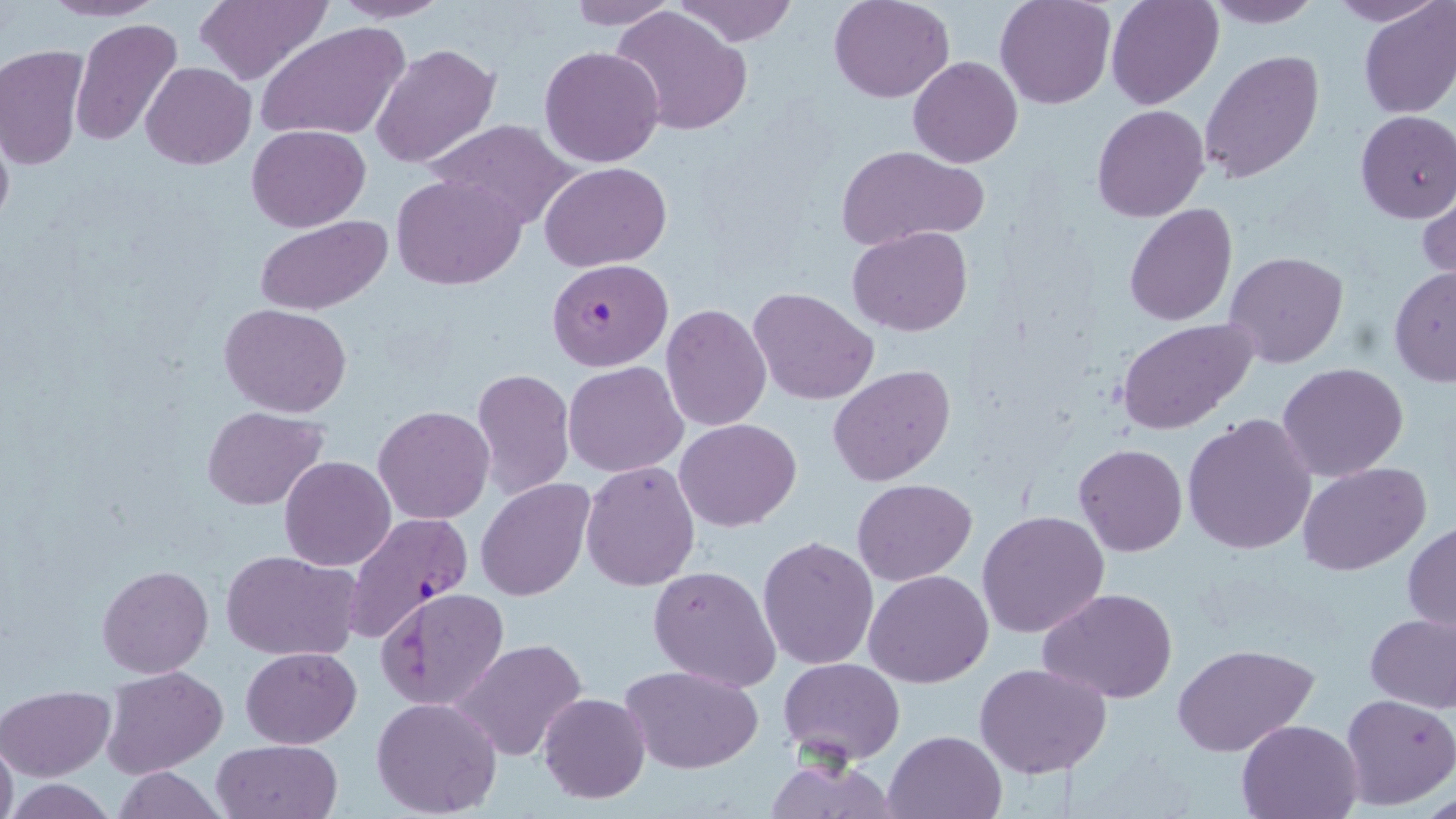 Approximate bounding boxes as [x1, y1, x2, y2] in pixels. Uninfected red blood cell locations: [38, 0, 166, 22], [193, 0, 330, 86], [328, 0, 454, 23], [674, 0, 800, 46], [830, 0, 955, 103], [995, 0, 1114, 110], [1106, 0, 1222, 110], [1203, 0, 1326, 28], [1324, 0, 1446, 25], [561, 1, 680, 28], [1357, 1, 1456, 119], [611, 5, 754, 136], [70, 19, 184, 145], [255, 22, 410, 144], [371, 43, 500, 170], [540, 44, 666, 167], [1, 45, 89, 174], [1199, 50, 1325, 185], [908, 57, 1023, 168], [141, 63, 255, 169], [1091, 104, 1210, 222], [1355, 111, 1456, 223], [0, 113, 15, 239], [426, 119, 576, 231], [246, 124, 370, 231], [834, 145, 990, 249], [540, 161, 671, 270], [394, 173, 527, 289], [1418, 184, 1456, 289], [1124, 204, 1238, 326], [252, 217, 394, 314], [847, 227, 973, 336], [1225, 250, 1348, 368], [1388, 265, 1456, 387], [748, 286, 877, 405], [219, 303, 352, 417], [661, 304, 772, 431], [1116, 317, 1258, 434], [563, 360, 688, 477], [1277, 363, 1408, 482], [829, 364, 956, 486], [473, 367, 574, 500], [374, 405, 494, 524], [201, 406, 329, 509], [1182, 414, 1316, 556], [675, 418, 801, 530], [1074, 443, 1188, 557], [280, 457, 395, 570], [580, 461, 701, 591], [1298, 463, 1431, 576], [477, 479, 596, 603], [852, 479, 976, 586], [977, 509, 1110, 639], [1403, 521, 1456, 633], [757, 535, 880, 670], [221, 549, 364, 661], [98, 564, 212, 677], [649, 565, 781, 692], [864, 568, 992, 687], [1039, 587, 1178, 704], [375, 589, 507, 711], [1365, 613, 1456, 711], [452, 638, 589, 762], [1173, 640, 1320, 756], [241, 646, 362, 747], [778, 657, 905, 766], [974, 662, 1113, 779], [620, 664, 765, 774], [101, 667, 227, 779], [0, 686, 113, 780], [537, 693, 650, 803], [1340, 693, 1455, 809], [371, 697, 502, 817], [1237, 717, 1363, 818], [884, 730, 1005, 819], [0, 734, 17, 819], [212, 739, 343, 819], [760, 758, 901, 817], [108, 767, 227, 819], [7, 779, 118, 817]. Plasmodium falciparum-infected red blood cell locations: [546, 258, 673, 371], [341, 511, 474, 642]. Slide-level diagnosis: Plasmodium falciparum. May-Grünwald-Giemsa-stained preparation. Captured at 1000x magnification. Image is 1456×819 pixels. Single field of view. Light microscopy. Thin blood smear.